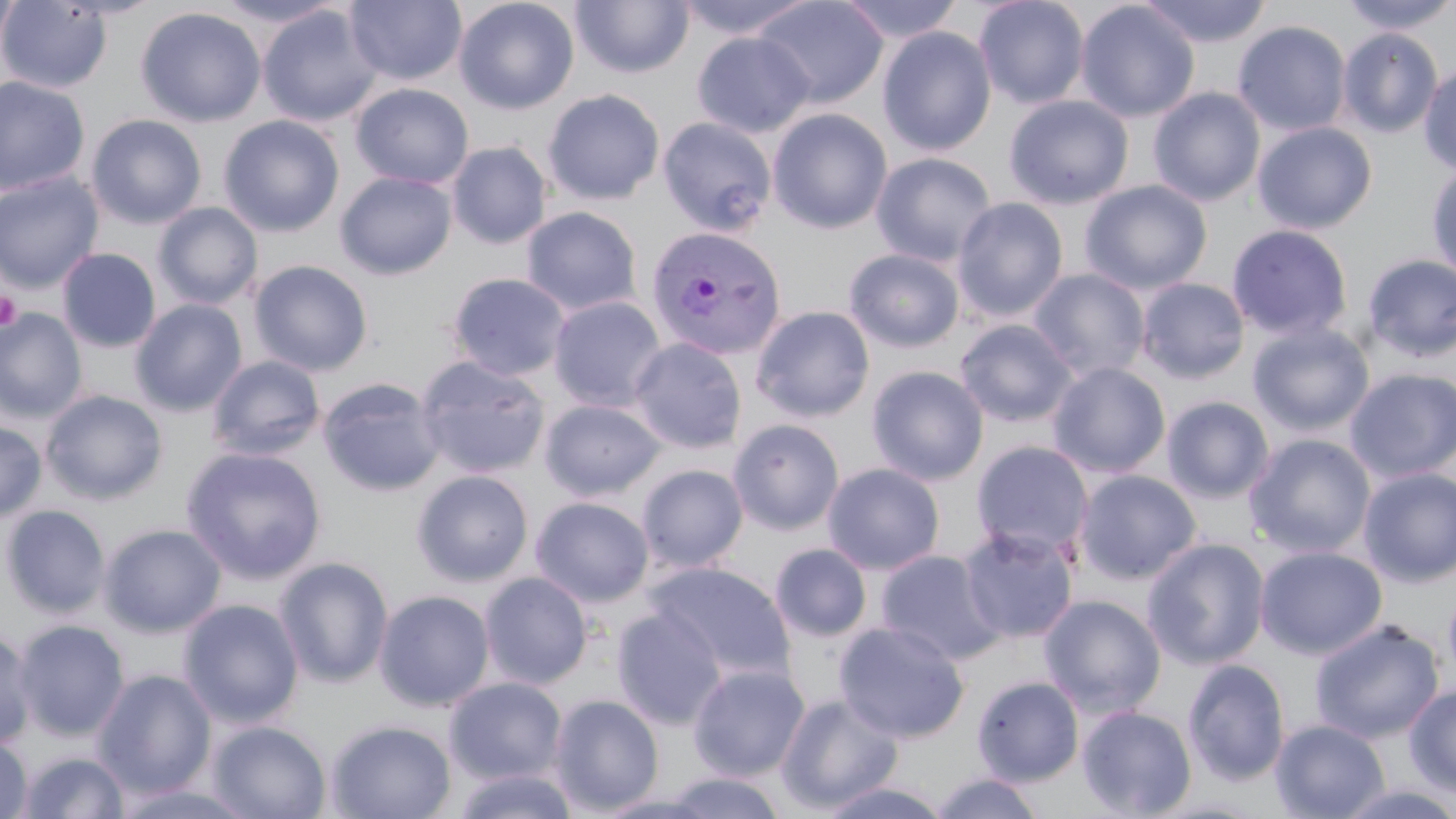

Plasmodium vivax-infected red blood cell locations = approximate bounding boxes as (x1, y1, x2, y2) in pixels: (645, 225, 787, 362)
slide-level diagnosis = Plasmodium vivax
modality = optical microscopy
field of view = one of a larger specimen
uninfected red blood cell locations = approximate bounding boxes as (x1, y1, x2, y2) in pixels: (0, 0, 20, 65), (214, 0, 345, 27), (453, 0, 579, 115), (675, 0, 817, 41), (752, 0, 889, 109), (836, 0, 966, 44), (973, 0, 1091, 109), (1137, 0, 1274, 48), (1339, 0, 1456, 36), (0, 1, 113, 93), (344, 1, 467, 86), (570, 1, 695, 78), (1075, 1, 1200, 122), (257, 5, 383, 127), (135, 6, 267, 127), (1232, 20, 1352, 136), (877, 26, 997, 156), (1337, 28, 1443, 138), (691, 31, 816, 138), (1419, 63, 1456, 176), (0, 76, 90, 196), (350, 83, 474, 189), (1148, 87, 1266, 207), (542, 89, 665, 205), (1003, 94, 1135, 209), (767, 108, 893, 234), (86, 114, 207, 229), (218, 115, 345, 237), (656, 116, 778, 238), (1252, 122, 1378, 234), (447, 141, 552, 249), (870, 152, 997, 267), (1426, 159, 1456, 284), (335, 171, 457, 279), (0, 172, 104, 293), (1079, 180, 1213, 295), (952, 197, 1069, 322), (153, 202, 263, 310), (521, 206, 643, 315), (1226, 224, 1353, 342), (56, 248, 161, 352), (843, 248, 966, 353), (1362, 253, 1456, 363), (249, 260, 373, 376), (1027, 268, 1151, 381), (446, 272, 572, 381), (1136, 278, 1250, 383), (548, 296, 667, 412), (131, 299, 247, 416), (750, 305, 875, 423), (0, 308, 87, 423), (955, 318, 1079, 428), (1248, 321, 1375, 437), (628, 336, 747, 453), (207, 355, 326, 461), (414, 355, 550, 479), (1047, 362, 1171, 478), (866, 365, 989, 485), (1345, 367, 1456, 482), (317, 377, 445, 497), (41, 390, 168, 505), (1161, 396, 1275, 503), (539, 398, 667, 501), (727, 418, 845, 536), (0, 421, 46, 522), (1244, 433, 1377, 558), (971, 441, 1094, 559), (181, 446, 327, 584), (822, 462, 945, 574), (637, 464, 747, 572), (1357, 466, 1456, 587), (411, 469, 534, 587), (1073, 469, 1202, 585), (530, 496, 654, 607), (1, 504, 111, 618), (100, 523, 226, 637), (957, 525, 1080, 645), (1141, 537, 1270, 671), (769, 543, 872, 642), (1255, 545, 1388, 659), (875, 550, 1004, 665), (274, 557, 394, 688), (646, 561, 796, 683), (479, 571, 593, 689), (1443, 583, 1456, 689), (374, 589, 494, 712), (1039, 594, 1167, 717), (178, 598, 304, 728), (611, 606, 728, 729), (13, 619, 130, 741), (1310, 619, 1445, 743), (833, 620, 970, 743), (0, 626, 37, 750), (1182, 658, 1290, 786), (687, 663, 810, 781), (94, 669, 217, 798), (971, 675, 1084, 787), (444, 677, 567, 784), (1404, 684, 1456, 797), (775, 693, 904, 813), (549, 694, 665, 815), (1076, 705, 1198, 818), (326, 719, 456, 819), (1270, 719, 1390, 819), (207, 721, 331, 819), (0, 735, 32, 819), (17, 751, 132, 818), (451, 767, 581, 819), (657, 771, 790, 818), (928, 772, 1047, 818), (815, 780, 952, 819), (108, 781, 263, 819), (1335, 783, 1456, 819)
platelet locations = approximate bounding boxes as (x1, y1, x2, y2) in pixels: (0, 291, 22, 332)
preparation = thin blood film
magnification = 1000x
image size = 1456×819 pixels
stain = May-Grünwald-Giemsa